Assess the morphology of the erythrocytes.
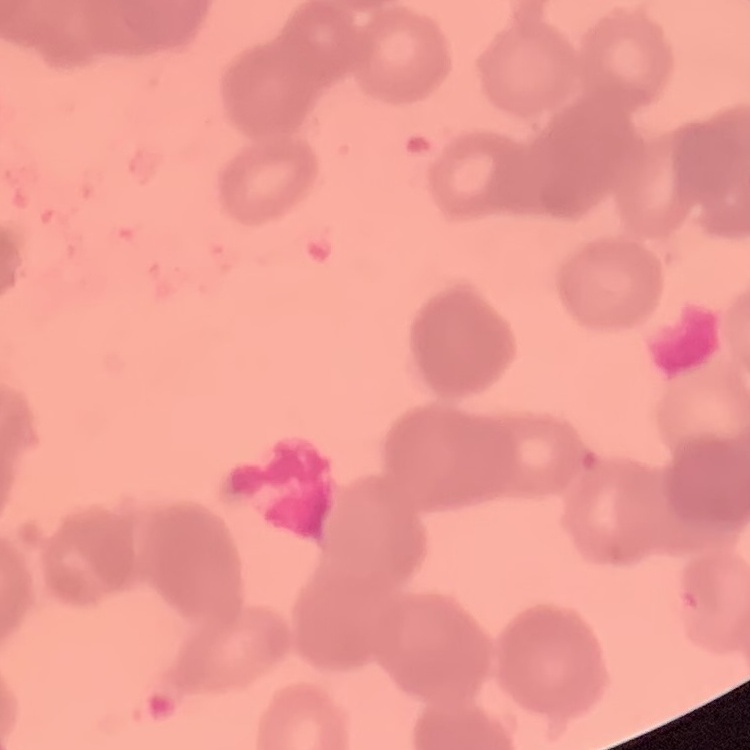
They show rouleaux formation.

Thin peripheral smear. Stained with either Field's or Giemsa. Square crop of a larger photomicrograph.